Outline each Babesia divergens-infected red blood cell.
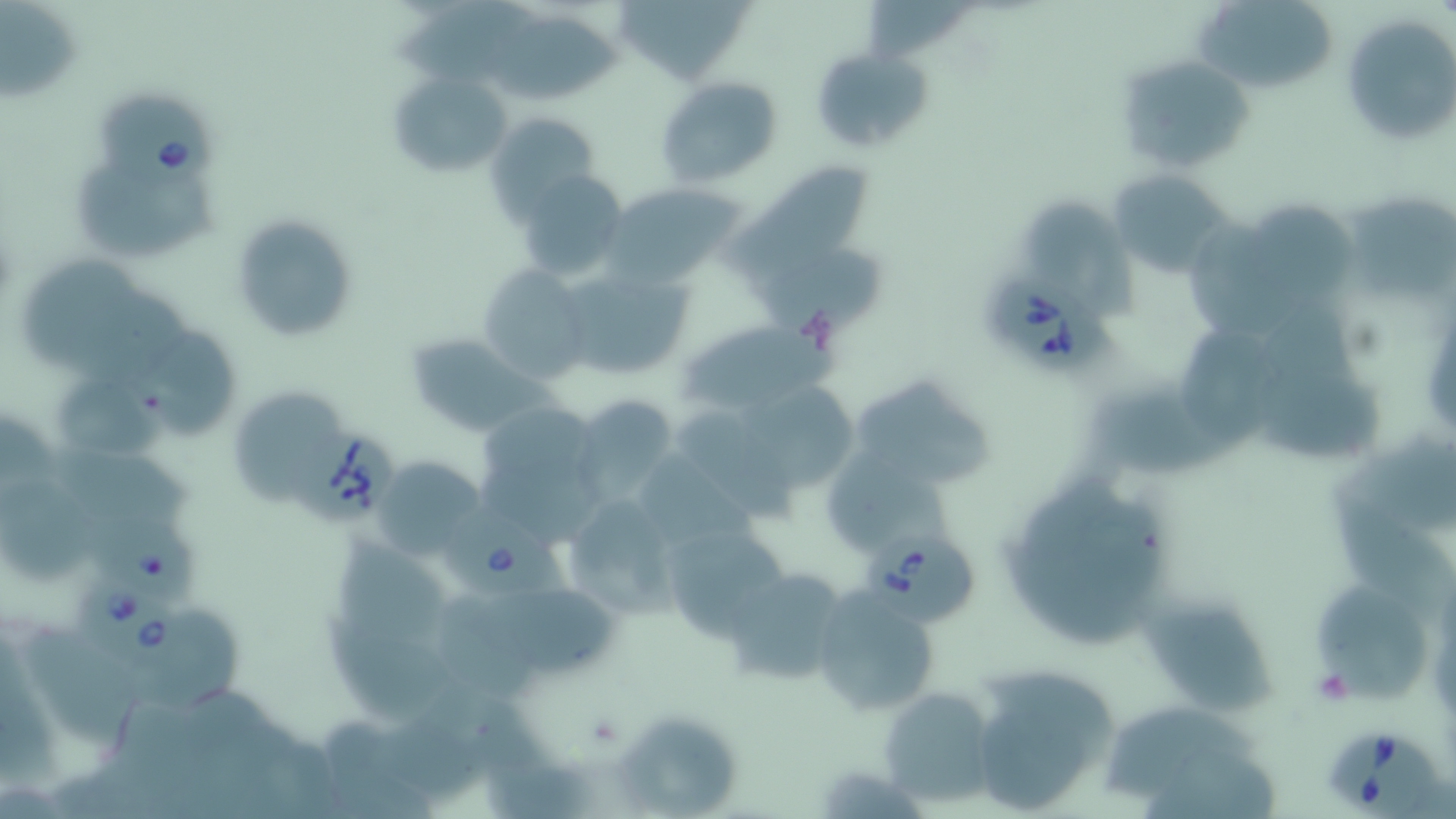
Approximate bounding boxes as (x1,y1)-(x2,y2) corner pairs in pixels.
Babesia divergens-infected red blood cells: (99,92)-(227,199), (984,273)-(1117,374), (278,418)-(395,523), (435,500)-(585,608), (859,528)-(978,627), (76,576)-(186,665), (1322,724)-(1442,816).

Uninfected red blood cell locations: (619,0)-(748,81), (861,0)-(972,60), (1199,2)-(1338,98), (1,4)-(84,104), (389,4)-(546,82), (485,12)-(629,109), (1341,13)-(1456,147), (1117,54)-(1257,176), (818,55)-(934,151), (390,70)-(512,181), (656,75)-(782,186), (485,112)-(597,215), (726,158)-(873,289), (71,161)-(227,263), (516,169)-(631,280), (1106,169)-(1239,276), (605,181)-(747,286), (1346,189)-(1456,300), (1025,197)-(1142,327), (1248,201)-(1358,299), (228,212)-(358,342), (1187,214)-(1299,341), (756,252)-(889,341), (25,255)-(142,375), (558,263)-(693,379), (477,265)-(590,384), (676,319)-(826,420), (1181,326)-(1276,449), (129,329)-(241,440), (403,332)-(540,437), (1257,368)-(1385,464), (848,371)-(993,488), (55,373)-(173,466), (229,384)-(338,495), (734,387)-(861,487), (571,396)-(682,510), (475,400)-(608,536), (674,416)-(800,529), (1339,440)-(1456,534), (44,442)-(205,537), (821,450)-(962,549), (372,456)-(485,557), (996,469)-(1176,647), (0,479)-(101,583), (559,496)-(684,623), (1333,504)-(1456,632), (660,521)-(791,640), (335,536)-(450,653), (720,565)-(853,685), (808,585)-(942,718), (1315,588)-(1425,706), (508,591)-(623,686), (431,597)-(549,701), (1144,599)-(1282,720), (137,609)-(250,712), (320,620)-(451,727), (16,629)-(153,756), (967,663)-(1121,816), (877,685)-(998,808), (1105,703)-(1271,796), (617,710)-(739,816). Platelet locations: (1311,669)-(1353,706). Slide-level diagnosis: Babesia divergens. May-Grünwald-Giemsa-stained preparation. Single field of view. Captured at 1000x magnification. Image is 1456×819 pixels. Thin blood smear. Light microscopy.